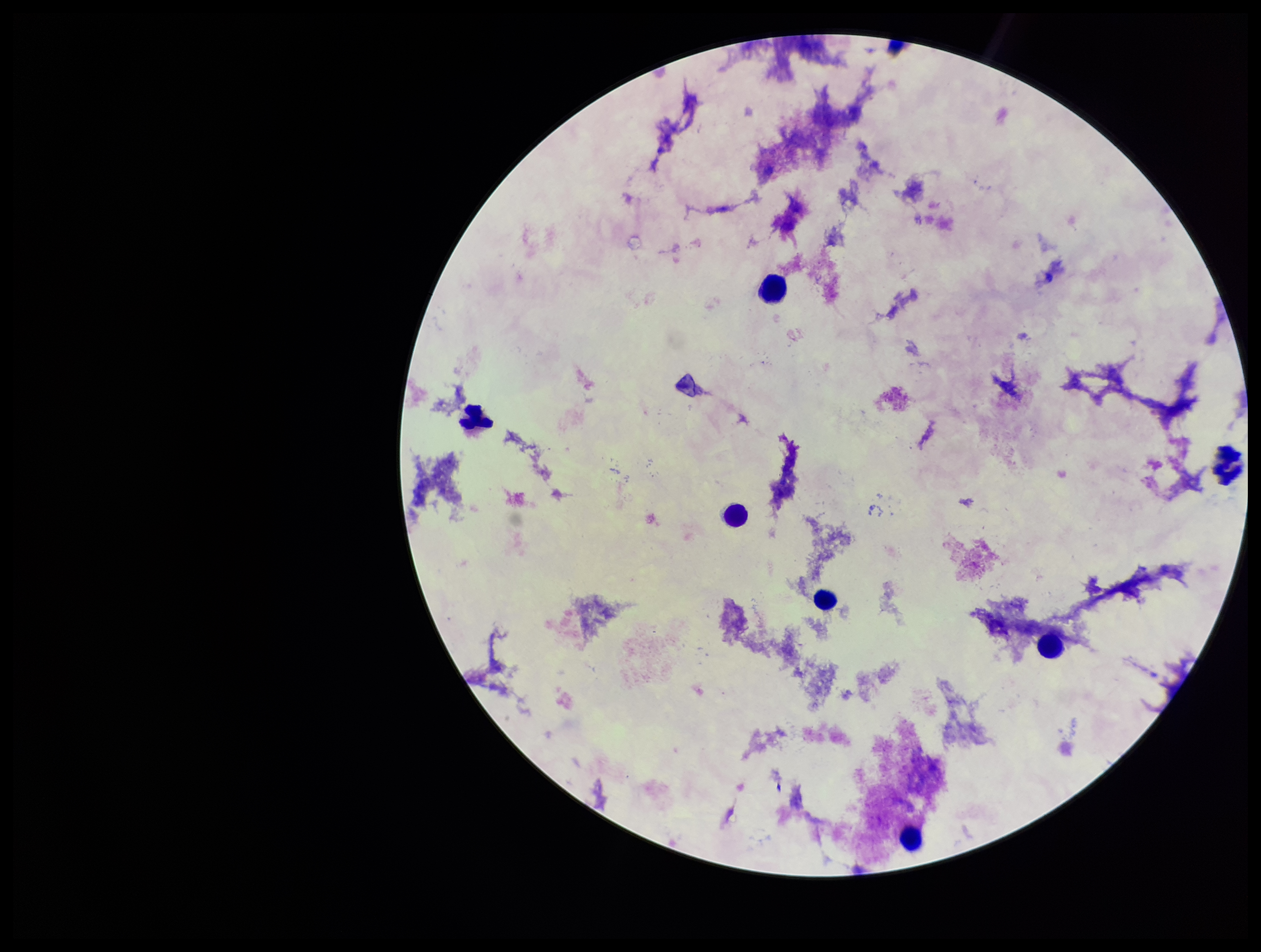
{
  "image_size": "1261×952 pixels",
  "patient_malaria_status": "negative",
  "leukocyte_count": 7,
  "parasite_count": 0,
  "preparation": "thick blood smear",
  "capture": "smartphone photograph through the microscope eyepiece",
  "field_of_view": "single",
  "plasmodium_parasites": "none identified",
  "stain": "Giemsa"
}